Assess the morphology of the erythrocytes.
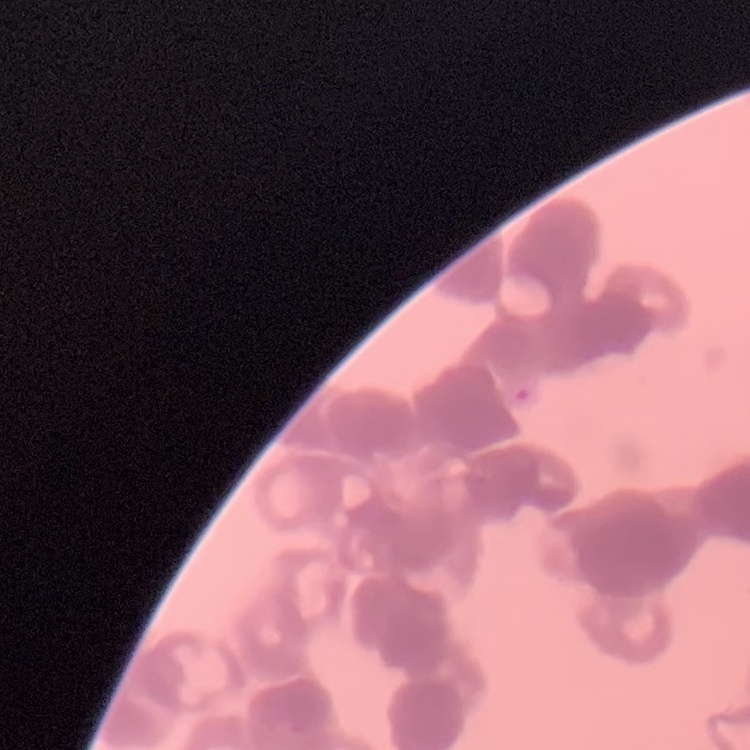

Rouleaux formation.

preparation = thin blood film
image type = square crop of a larger photomicrograph
stain = Field's or Giemsa